Classify this cell by malaria status.
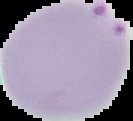
It is parasitized.

Segmented cell region on a black background. Image is 133×121 pixels. From a thin blood film.